Assess this cell for malaria.
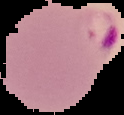

Parasitized.

image size = 124×115 pixels
image type = segmented cell region on a black background
preparation = thin blood film